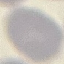
Summary:
  - Result: no malaria parasites detected
  - Capture: smartphone through the microscope eyepiece
  - Preparation: thin smear
  - Stain: Giemsa
  - Image type: cell patch, automatically extracted from a larger field of view and resized to 64 × 64 pixels